Locate every Plasmodium vivax-infected red blood cell.
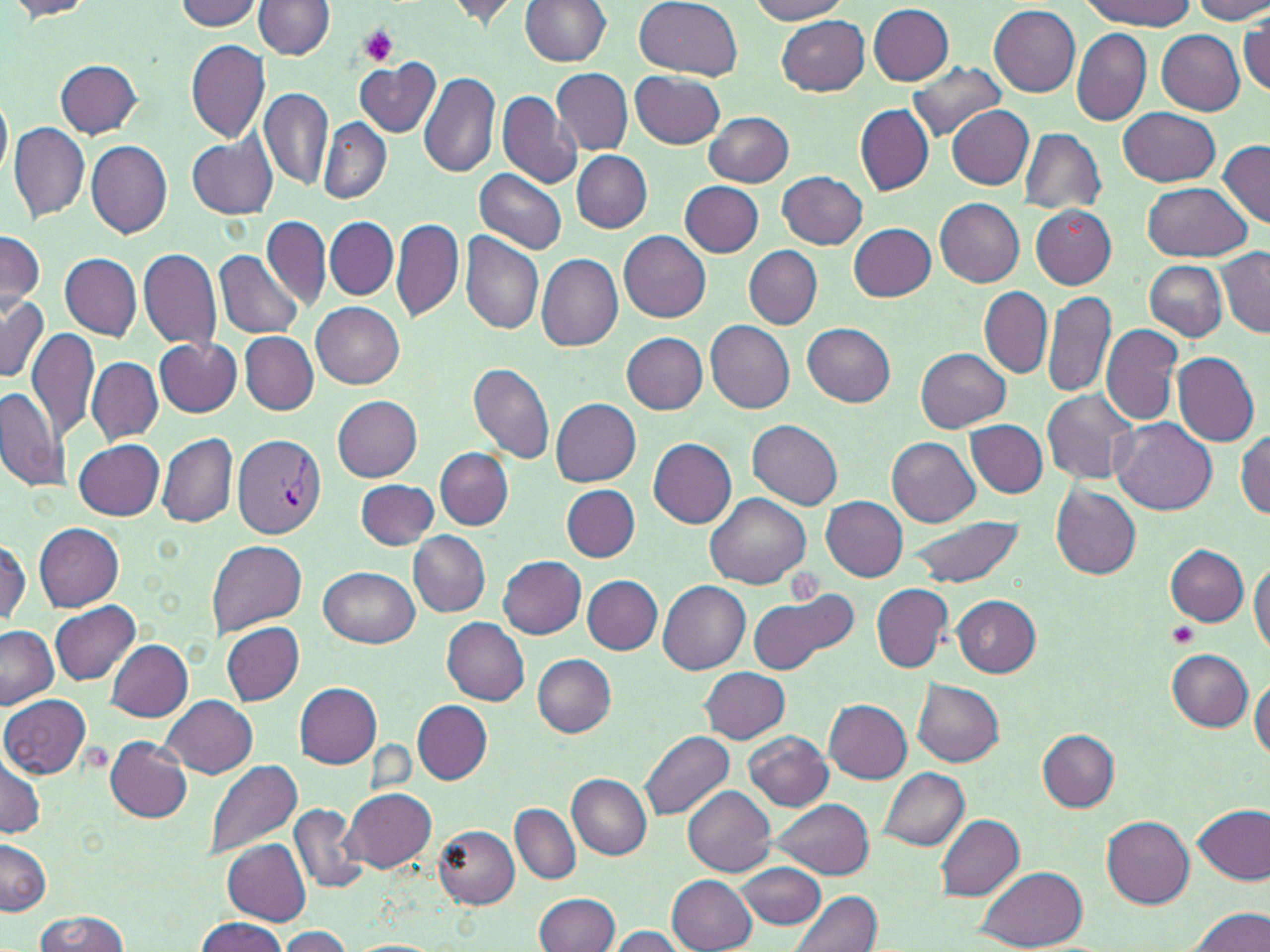
Approximate bounding boxes as [x1, y1, x2, y2] in pixels.
Plasmodium vivax-infected red blood cells: [233, 433, 326, 538].

slide_level_diagnosis: Plasmodium vivax
stain: May-Grünwald-Giemsa
platelet_locations: 'approximate bounding boxes as [x1, y1, x2, y2] in pixels: [355, 23, 401, 67], [1168, 624, 1198, 649]'
modality: light microscopy
image_size: 1270×952 pixels
uninfected_red_blood_cell_locations: 'approximate bounding boxes as [x1, y1, x2, y2] in pixels: [4, 0, 100, 19], [521, 0, 612, 67], [635, 0, 742, 79], [749, 0, 852, 22], [1190, 0, 1270, 23], [173, 1, 264, 30], [253, 1, 335, 58], [442, 1, 529, 28], [1078, 1, 1195, 29], [867, 3, 953, 85], [990, 5, 1081, 97], [776, 14, 870, 94], [1240, 17, 1270, 97], [1071, 28, 1151, 125], [1157, 30, 1245, 115], [185, 39, 271, 143], [354, 59, 440, 137], [369, 59, 478, 163], [56, 60, 143, 137], [905, 61, 1006, 140], [551, 68, 633, 153], [418, 71, 500, 180], [631, 71, 725, 147], [259, 87, 333, 188], [496, 90, 582, 190], [0, 91, 11, 185], [854, 105, 933, 196], [947, 105, 1034, 189], [1120, 108, 1220, 185], [705, 111, 794, 187], [319, 120, 390, 204], [10, 121, 90, 224], [24, 121, 147, 237], [1020, 128, 1106, 213], [188, 136, 277, 219], [1218, 138, 1269, 227], [86, 140, 173, 237], [571, 151, 652, 232], [474, 167, 567, 255], [777, 171, 867, 248], [679, 180, 765, 257], [1141, 182, 1254, 260], [935, 198, 1024, 288], [1030, 206, 1116, 289], [262, 215, 331, 312], [325, 217, 399, 300], [391, 217, 465, 324], [849, 223, 936, 301], [0, 230, 44, 315], [618, 230, 711, 321], [460, 231, 544, 334], [138, 247, 222, 349], [744, 247, 822, 329], [1217, 247, 1269, 338], [215, 250, 305, 339], [60, 252, 142, 339], [535, 253, 623, 352], [1144, 260, 1227, 341], [979, 287, 1052, 378], [1042, 289, 1115, 398], [0, 294, 50, 382], [311, 302, 404, 388], [1041, 304, 1176, 413], [705, 320, 795, 413], [802, 321, 896, 406], [1101, 324, 1182, 428], [27, 327, 99, 440], [242, 332, 318, 414], [620, 332, 708, 413], [155, 337, 242, 416], [915, 347, 1009, 431], [1174, 352, 1259, 447], [87, 358, 163, 445], [468, 361, 556, 467], [0, 383, 71, 496], [1044, 390, 1139, 484], [332, 395, 423, 480], [550, 398, 641, 487], [966, 419, 1048, 497], [748, 420, 843, 510], [1114, 420, 1215, 515], [1236, 431, 1269, 516], [159, 433, 237, 529], [887, 436, 980, 527], [648, 438, 737, 529], [75, 439, 165, 519], [436, 447, 513, 529], [357, 480, 439, 550], [561, 485, 638, 561], [1050, 485, 1142, 579], [705, 493, 811, 589], [820, 496, 907, 581], [905, 512, 1025, 590], [34, 523, 124, 610], [409, 532, 491, 616], [0, 537, 29, 626], [207, 539, 307, 635], [1166, 544, 1250, 626], [498, 555, 587, 640], [1249, 561, 1270, 656], [321, 566, 418, 647], [584, 576, 661, 655], [658, 580, 750, 674], [871, 584, 952, 672], [748, 588, 853, 674], [952, 595, 1040, 676], [50, 601, 143, 685], [441, 617, 530, 705], [221, 621, 304, 704], [0, 625, 58, 710], [105, 638, 192, 721], [1167, 648, 1252, 730], [533, 654, 617, 736], [699, 667, 790, 742], [1250, 678, 1270, 764], [913, 680, 1003, 767], [295, 683, 382, 768], [0, 693, 91, 778], [161, 696, 258, 777], [824, 699, 911, 781], [412, 701, 492, 784], [642, 729, 734, 820], [1037, 729, 1119, 810], [743, 731, 831, 810], [105, 738, 192, 823], [0, 753, 46, 840], [203, 758, 303, 860], [879, 767, 969, 850], [566, 774, 652, 859], [683, 785, 776, 876], [343, 788, 437, 873], [769, 799, 874, 878], [288, 802, 368, 892], [509, 804, 580, 885], [1192, 805, 1270, 885], [935, 813, 1025, 902], [1101, 816, 1195, 910], [435, 825, 520, 908], [222, 838, 311, 926], [1, 839, 51, 916], [737, 861, 828, 930], [976, 867, 1089, 951], [667, 875, 757, 952], [790, 891, 883, 952], [534, 893, 620, 952], [1187, 907, 1269, 952], [34, 910, 130, 952], [195, 917, 286, 952], [279, 926, 352, 950], [608, 926, 685, 951], [346, 939, 442, 952]'
preparation: thin blood film
field_of_view: single
magnification: 1000x